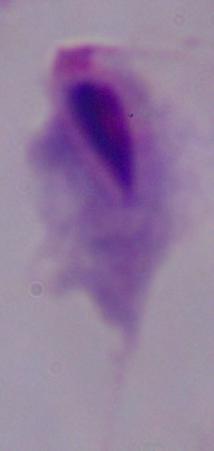
identification = trichomonad
modality = photomicrograph
magnification = 1000x